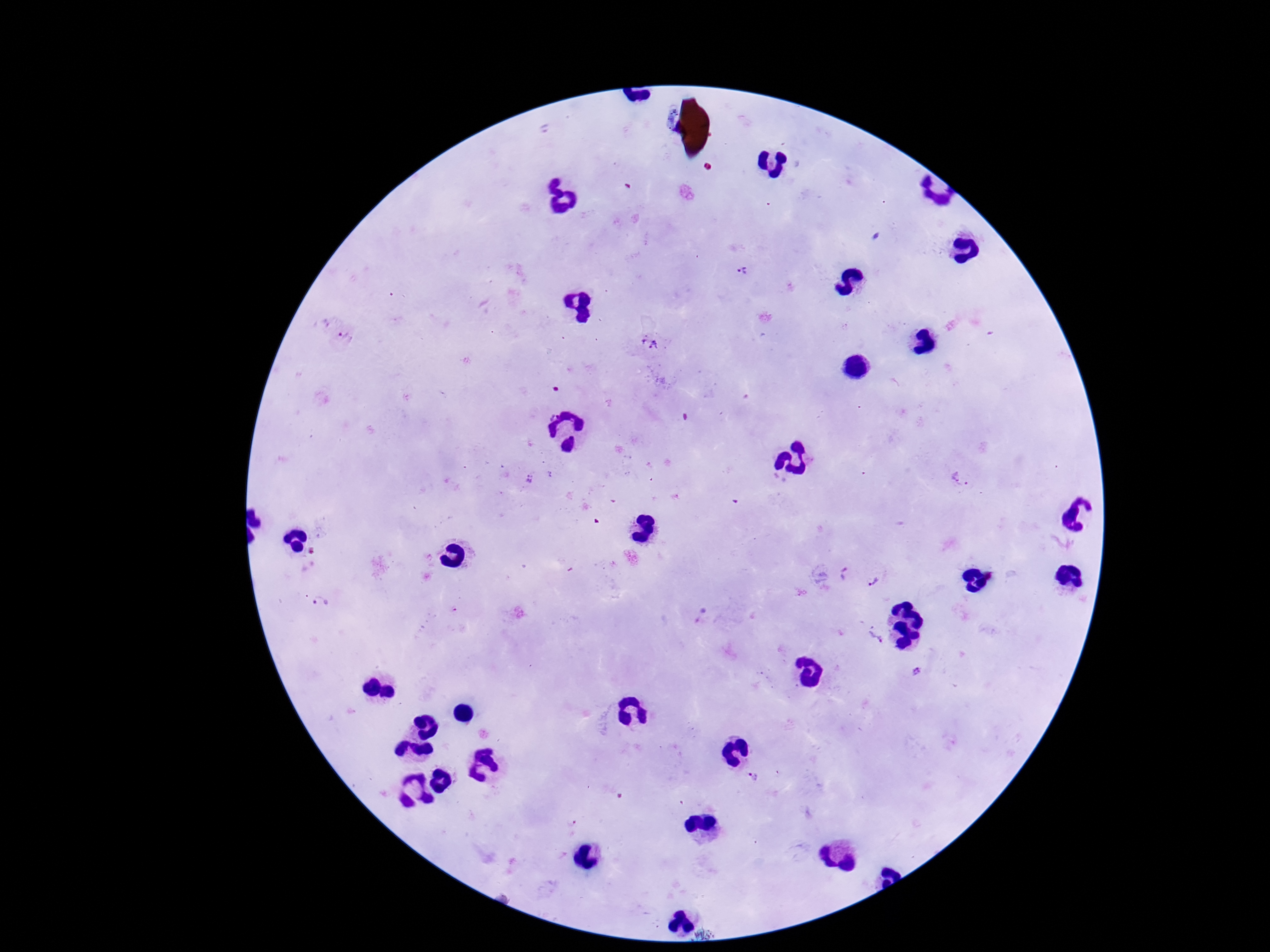

Approximate centers as {x, y} in pixels.
Summary:
  - Plasmodium parasite locations: {548, 127}, {743, 275}, {345, 339}, {649, 345}, {549, 413}, {552, 475}, {963, 477}, {529, 479}, {846, 573}, {875, 581}, {321, 602}, {874, 638}, {916, 672}, {755, 777}
  - Magnification: 100x
  - Patient malaria status: positive
  - Field of view: one from this slide
  - Preparation: thick peripheral-blood smear
  - Stain: Giemsa
  - Capture: smartphone camera through the microscope eyepiece
  - Image size: 1270×952 pixels